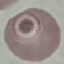

Malaria status: uninfected. Automatically extracted cell patch, resized to 64 × 64 pixels. Acquired by smartphone through the microscope eyepiece. Giemsa-stained preparation. Thin smear of blood.